Name the parasite shown.
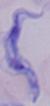
This is a trypanosome.

Summary:
  - Modality: micrograph
  - Magnification: 1000x